Look for Plasmodium parasites.
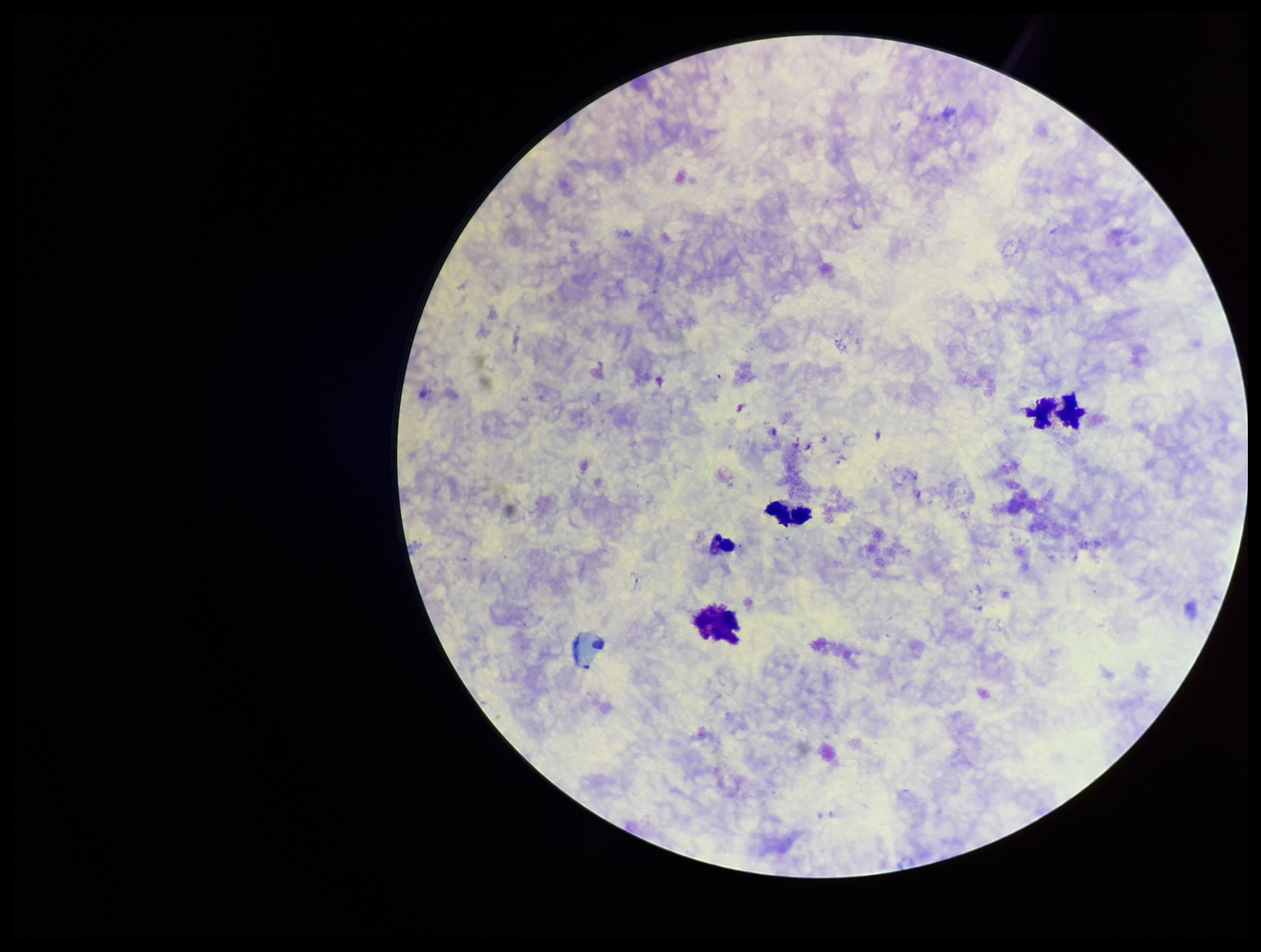

None seen.

Summary:
  - Image size: 1261×952 pixels
  - Preparation: thick smear
  - Parasite count: 0
  - Leukocyte count: 3
  - Patient malaria status: negative
  - Field of view: single
  - Capture: smartphone photograph through the microscope eyepiece
  - Stain: Giemsa